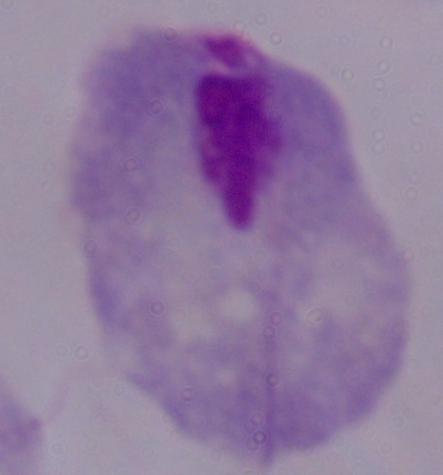

Summary:
  - Modality: photomicrograph
  - Identification: trichomonad
  - Magnification: 1000x